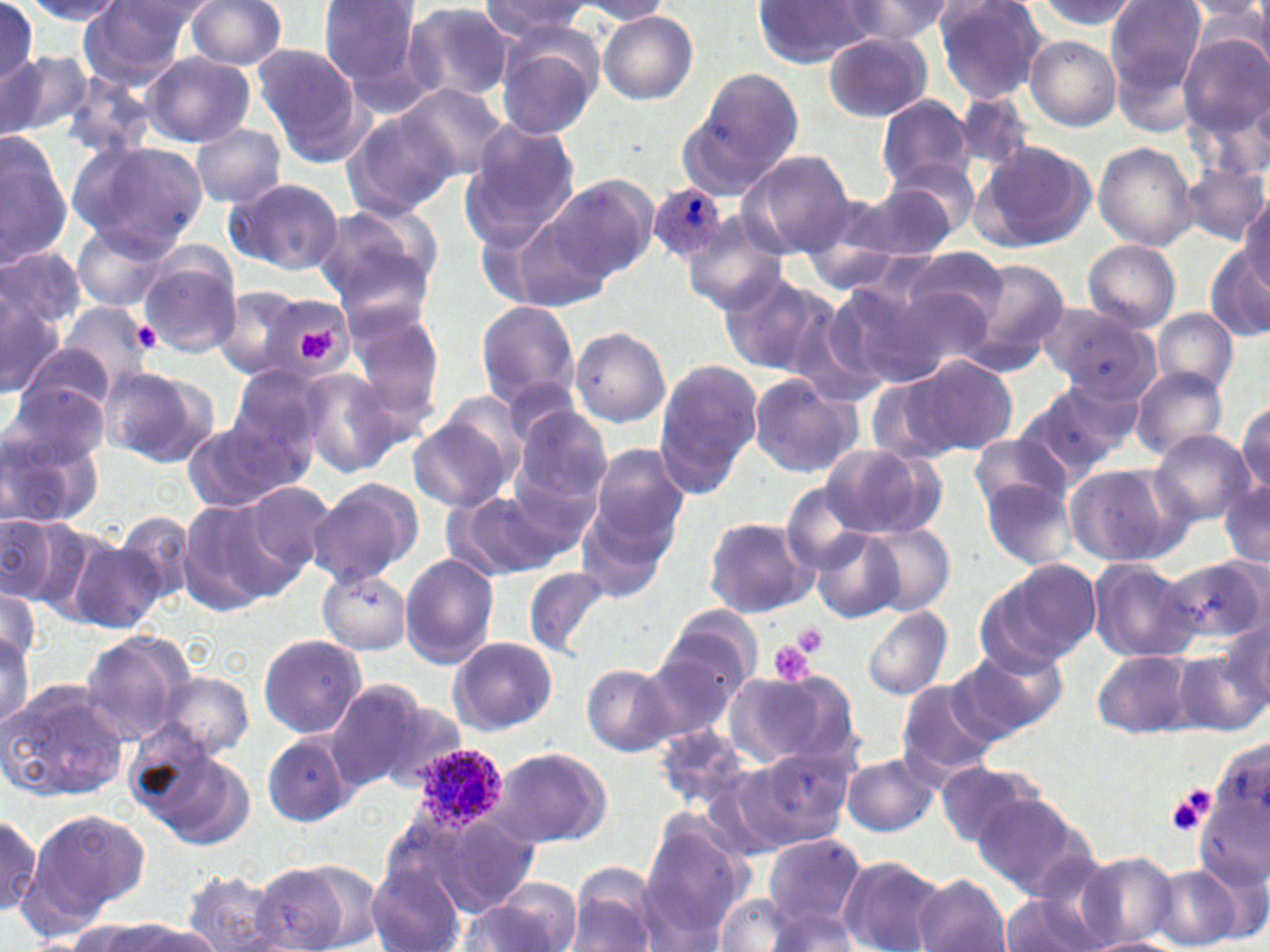
plasmodium_ovale_infected_red_blood_cell_locations: 'approximate bounding boxes as (x1,y1)-(x2,y2) corner pairs in pixels: (649,185)-(728,264), (414,744)-(506,835)'
slide_level_diagnosis: Plasmodium ovale
preparation: thin blood film
modality: light microscopy
magnification: 1000x
uninfected_red_blood_cell_locations: 'approximate bounding boxes as (x1,y1)-(x2,y2) corner pairs in pixels: (22,0)-(127,24), (183,0)-(288,70), (318,0)-(424,94), (480,0)-(596,38), (1032,0)-(1140,31), (1181,0)-(1269,24), (1238,0)-(1270,75), (574,1)-(675,25), (840,1)-(954,42), (933,1)-(1050,105), (1106,1)-(1205,94), (751,2)-(881,67), (77,3)-(197,86), (401,3)-(516,104), (1186,3)-(1268,45), (0,4)-(39,86), (598,11)-(699,105), (275,16)-(399,141), (494,32)-(602,139), (823,32)-(932,122), (1177,33)-(1270,138), (1024,36)-(1120,131), (254,46)-(365,160), (0,50)-(89,141), (141,54)-(255,148), (681,69)-(803,192), (56,71)-(161,162), (396,84)-(508,182), (877,95)-(975,190), (341,109)-(456,220), (457,120)-(580,247), (191,124)-(287,208), (0,135)-(69,271), (70,140)-(208,256), (977,141)-(1097,251), (1093,141)-(1198,250), (738,151)-(854,259), (884,160)-(980,239), (1183,164)-(1268,246), (549,173)-(659,281), (222,176)-(345,277), (859,177)-(968,262), (796,191)-(907,293), (1241,195)-(1270,292), (311,206)-(441,319), (503,210)-(612,317), (682,217)-(789,317), (70,223)-(170,312), (1082,240)-(1180,331), (901,245)-(1018,340), (0,246)-(87,335), (1207,247)-(1270,342), (136,252)-(240,356), (953,257)-(1071,369), (722,271)-(834,379), (822,280)-(943,392), (213,284)-(327,384), (0,292)-(65,400), (270,301)-(355,377), (476,301)-(580,409), (55,302)-(156,392), (1041,305)-(1159,401), (348,306)-(449,441), (1153,307)-(1238,395), (569,327)-(671,429), (19,345)-(119,424), (909,355)-(1018,456), (654,360)-(762,494), (102,365)-(217,466), (296,366)-(408,477), (227,367)-(327,472), (1131,367)-(1228,462), (1053,368)-(1152,453), (745,374)-(863,479), (865,374)-(962,467), (6,382)-(108,475), (1010,386)-(1123,484), (1235,401)-(1269,496), (513,409)-(612,514), (407,415)-(514,513), (183,416)-(304,514), (0,427)-(99,529), (969,430)-(1076,516), (1149,430)-(1255,526), (586,440)-(691,554), (815,442)-(943,541), (1064,462)-(1183,567), (978,474)-(1079,569), (308,477)-(422,585), (1218,478)-(1269,571), (237,481)-(336,581), (780,484)-(877,576), (443,490)-(561,582), (176,499)-(285,614), (575,500)-(676,607), (114,509)-(195,609), (1,513)-(70,605), (702,516)-(816,618), (864,523)-(956,614), (810,530)-(904,624), (66,537)-(166,634), (399,554)-(500,668), (1168,556)-(1267,645), (1088,559)-(1200,662), (978,562)-(1098,672), (523,566)-(609,660), (317,567)-(412,654), (0,586)-(41,672), (659,606)-(762,702), (863,606)-(951,700), (1220,616)-(1270,712), (0,627)-(33,733), (79,631)-(195,748), (257,633)-(367,739), (447,635)-(558,735), (949,646)-(1066,741), (636,648)-(740,744), (1093,649)-(1196,738), (1175,649)-(1265,736), (582,662)-(676,755), (723,667)-(858,772), (154,671)-(255,759), (0,679)-(130,805), (323,680)-(431,792), (895,680)-(998,780), (367,698)-(468,791), (262,734)-(353,828), (132,741)-(252,851), (486,745)-(613,850), (726,747)-(854,856), (841,753)-(938,836), (935,759)-(1042,849), (972,792)-(1090,898), (26,807)-(148,930), (0,808)-(47,922), (404,811)-(544,919), (637,814)-(752,940), (763,832)-(865,931), (1078,852)-(1177,947), (838,855)-(946,952), (249,862)-(360,952), (368,864)-(466,952), (569,865)-(659,952), (1152,866)-(1242,950), (181,869)-(290,951), (911,874)-(1011,952), (469,882)-(584,952), (1000,892)-(1102,952), (715,893)-(798,951), (765,907)-(858,951), (67,919)-(172,952), (113,919)-(223,951), (1085,936)-(1179,952)'
platelet_locations: 'approximate bounding boxes as (x1,y1)-(x2,y2) corner pairs in pixels: (129,316)-(163,354), (295,328)-(336,362), (789,620)-(831,658), (767,638)-(817,686), (1165,791)-(1211,839)'
stain: May-Grünwald-Giemsa
field_of_view: single
image_size: 1270×952 pixels